State the blood parasite species.
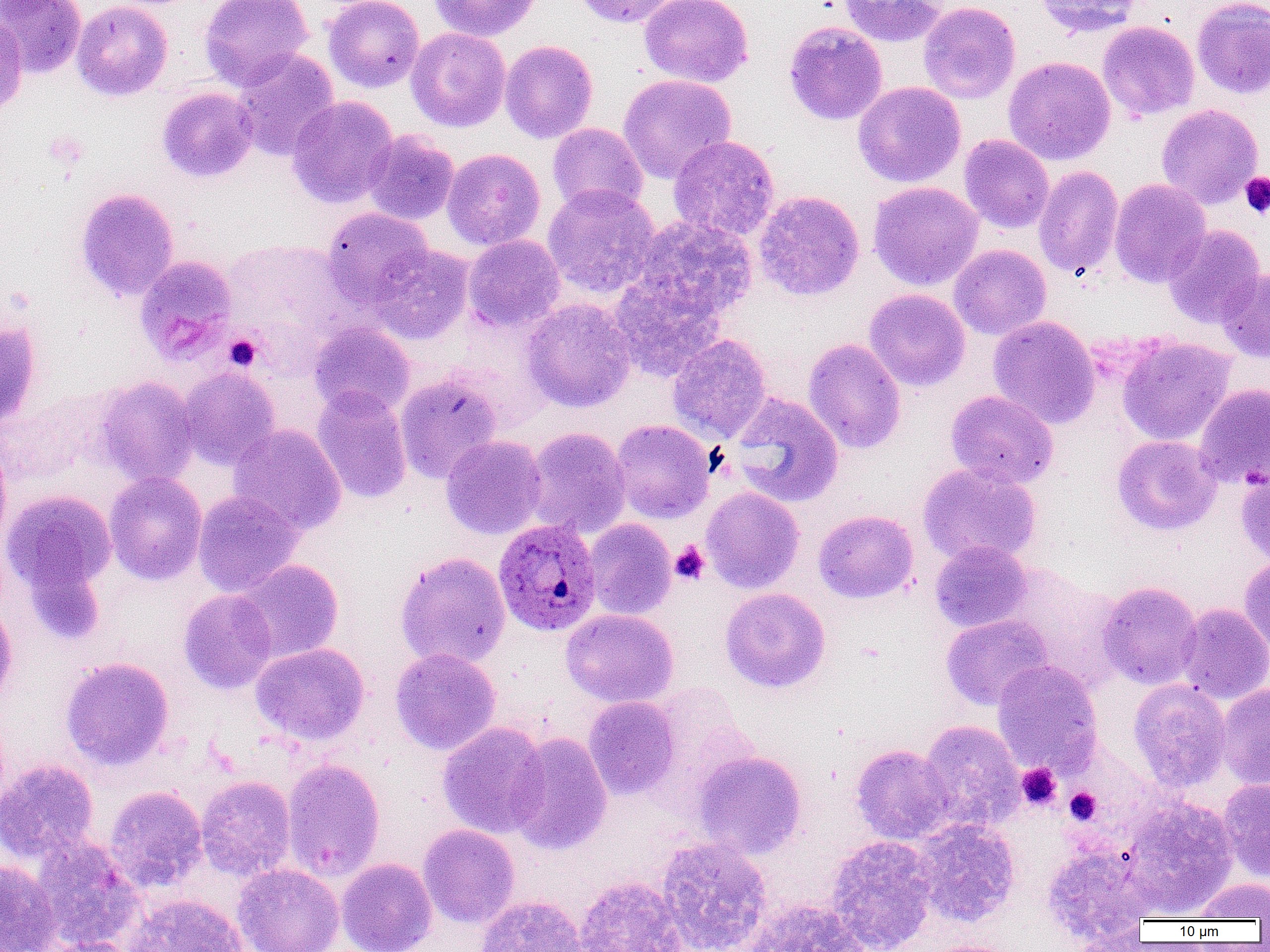

Plasmodium ovale.

{
  "field_of_view": "one of a larger specimen",
  "preparation": "thin blood film",
  "plasmodium_ovale_infected_red_blood_cell_locations": "approximate bounding boxes as (x1, y1, x2, y2) in pixels: (493, 518, 601, 637)",
  "image_size": "1270×952 pixels",
  "modality": "light microscopy",
  "platelet_locations": "approximate bounding boxes as (x1, y1, x2, y2) in pixels: (1240, 172, 1270, 219), (225, 334, 261, 371), (670, 541, 709, 584), (1016, 763, 1062, 811), (1064, 787, 1101, 825)",
  "uninfected_red_blood_cell_locations": "approximate bounding boxes as (x1, y1, x2, y2) in pixels: (0, 0, 86, 78), (71, 0, 172, 101), (200, 0, 313, 91), (323, 0, 425, 93), (427, 0, 541, 42), (573, 0, 684, 28), (639, 0, 754, 88), (837, 0, 948, 47), (1036, 0, 1144, 37), (1192, 0, 1270, 99), (918, 1, 1020, 104), (0, 16, 28, 118), (783, 21, 888, 125), (1097, 21, 1200, 121), (406, 27, 511, 132), (500, 40, 598, 143), (232, 49, 340, 161), (1003, 56, 1116, 165), (618, 74, 737, 184), (853, 81, 966, 188), (157, 86, 258, 182), (287, 96, 398, 208), (1156, 103, 1263, 208), (547, 123, 647, 216), (363, 130, 460, 225), (959, 134, 1055, 233), (668, 135, 780, 241), (442, 148, 546, 250), (1033, 166, 1124, 280), (1109, 179, 1211, 287), (868, 181, 984, 290), (542, 185, 661, 299), (76, 187, 179, 301), (753, 190, 865, 301), (322, 207, 435, 308), (631, 216, 758, 322), (1163, 225, 1265, 328), (463, 234, 565, 332), (948, 244, 1051, 340), (370, 246, 474, 344), (135, 255, 237, 363), (1217, 267, 1270, 363), (608, 273, 727, 380), (864, 288, 971, 391), (522, 299, 637, 412), (988, 315, 1101, 429), (0, 321, 41, 429), (308, 321, 416, 418), (667, 333, 772, 443), (1116, 336, 1236, 445), (803, 338, 906, 453), (177, 366, 280, 470), (395, 372, 503, 483), (94, 376, 200, 487), (1195, 383, 1270, 489), (312, 386, 412, 504), (945, 390, 1059, 488), (730, 392, 844, 507), (611, 419, 715, 524), (229, 423, 346, 536), (523, 427, 631, 540), (440, 435, 546, 539), (1112, 435, 1222, 535), (0, 438, 12, 554), (917, 463, 1042, 568), (1236, 467, 1270, 567), (104, 471, 207, 585), (701, 486, 804, 593), (2, 489, 117, 602), (193, 491, 303, 597), (813, 509, 919, 603), (584, 519, 677, 620), (930, 540, 1033, 633), (395, 552, 511, 670), (1239, 554, 1270, 657), (233, 560, 344, 663), (1097, 581, 1202, 689), (720, 587, 830, 692), (179, 588, 278, 694), (0, 598, 18, 706), (1177, 602, 1270, 704), (561, 608, 678, 707), (941, 614, 1053, 711), (251, 642, 369, 745), (390, 647, 501, 754), (60, 656, 174, 770), (992, 660, 1103, 775), (1129, 678, 1232, 791), (1216, 683, 1270, 790), (583, 696, 681, 800), (918, 719, 1024, 831), (437, 722, 550, 838), (507, 732, 612, 854), (851, 744, 953, 844), (693, 750, 807, 859), (282, 758, 385, 881), (0, 759, 99, 863), (196, 775, 296, 882), (1218, 778, 1270, 882), (104, 785, 208, 892), (1121, 797, 1239, 916), (911, 818, 1020, 927), (418, 824, 520, 928), (825, 835, 936, 952), (31, 836, 144, 949), (657, 836, 772, 952), (1041, 841, 1159, 942), (337, 857, 437, 952), (0, 859, 59, 952), (233, 863, 344, 952), (575, 875, 686, 952), (1190, 878, 1270, 921), (124, 893, 248, 952), (474, 895, 587, 952), (743, 899, 871, 952), (1066, 926, 1151, 952), (38, 937, 139, 952), (918, 939, 1023, 952)",
  "magnification": "1000x"
}